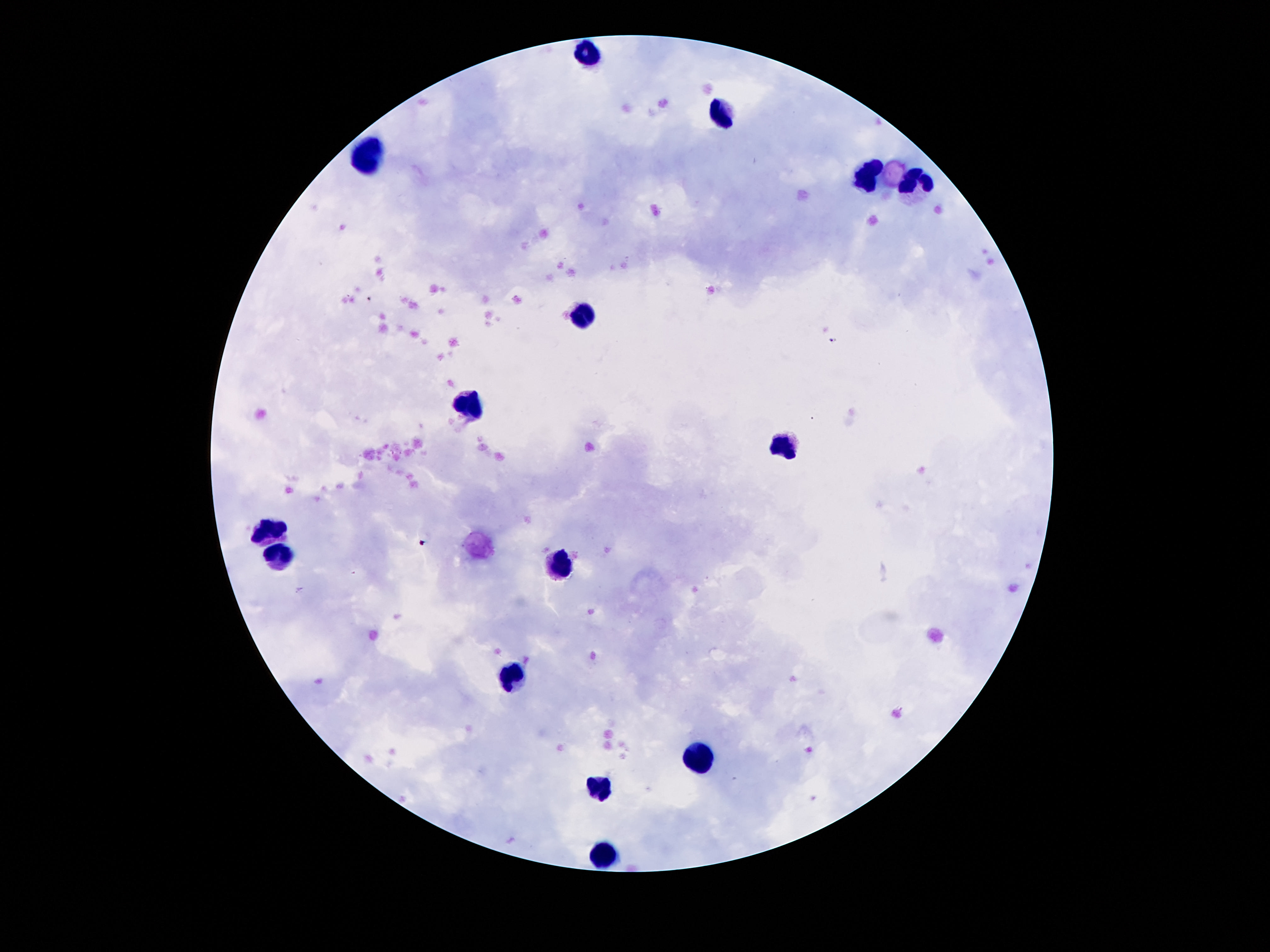

Approximate centers as (x, y) in pixels. Leukocyte locations: (592, 57), (722, 118), (366, 155), (868, 181), (917, 189), (583, 315), (464, 404), (784, 444), (271, 534), (282, 554), (559, 565), (512, 678), (698, 757), (599, 791), (599, 855). Giemsa-stained preparation. One field from this slide. Photographed through the microscope eyepiece with a smartphone camera. Patient malaria status: uninfected. Image is 1270×952 pixels. 100x magnification. Thick peripheral-blood smear.